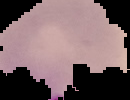 Image is 130×100 pixels. Result: malaria parasites detected. Segmented cell region on a black background. From a thin blood smear.